Classify this cell by malaria status.
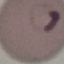

Parasitized.

capture = smartphone camera at the microscope eyepiece
stain = Giemsa
image type = automatically extracted cell patch, resized to 64 × 64 pixels
preparation = thin blood film